Locate every Plasmodium parasite.
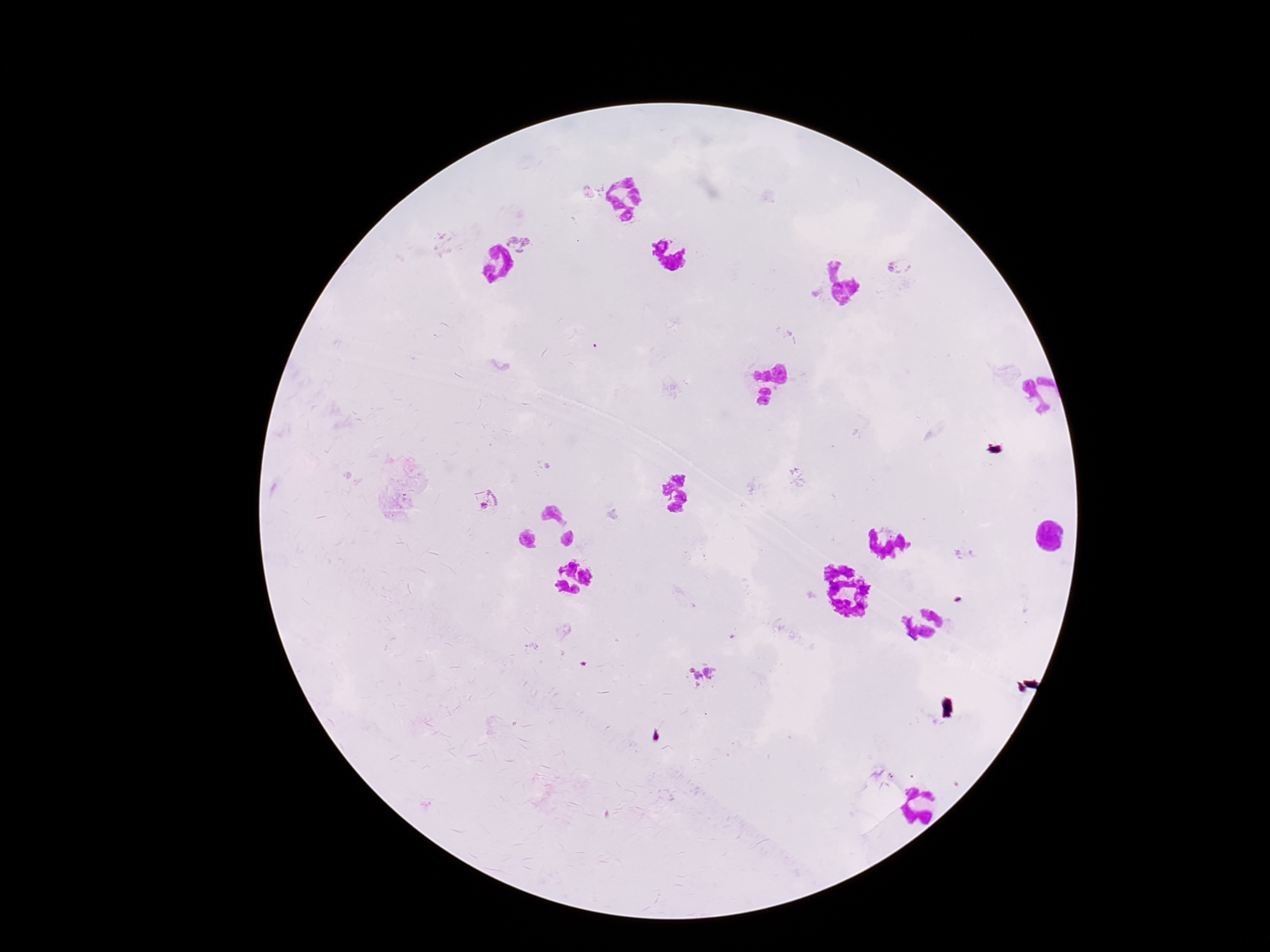
Approximate object centers, in pixels from the top-left corner.
Plasmodium parasites: (x=519, y=243), (x=901, y=266), (x=493, y=499), (x=693, y=670), (x=711, y=671), (x=698, y=676).

Patient malaria status: positive. Smartphone photograph taken through the microscope eyepiece. Thick blood film. 100x magnification. Single field of view. Image is 1270×952 pixels. Giemsa stain.